State the preparation type.
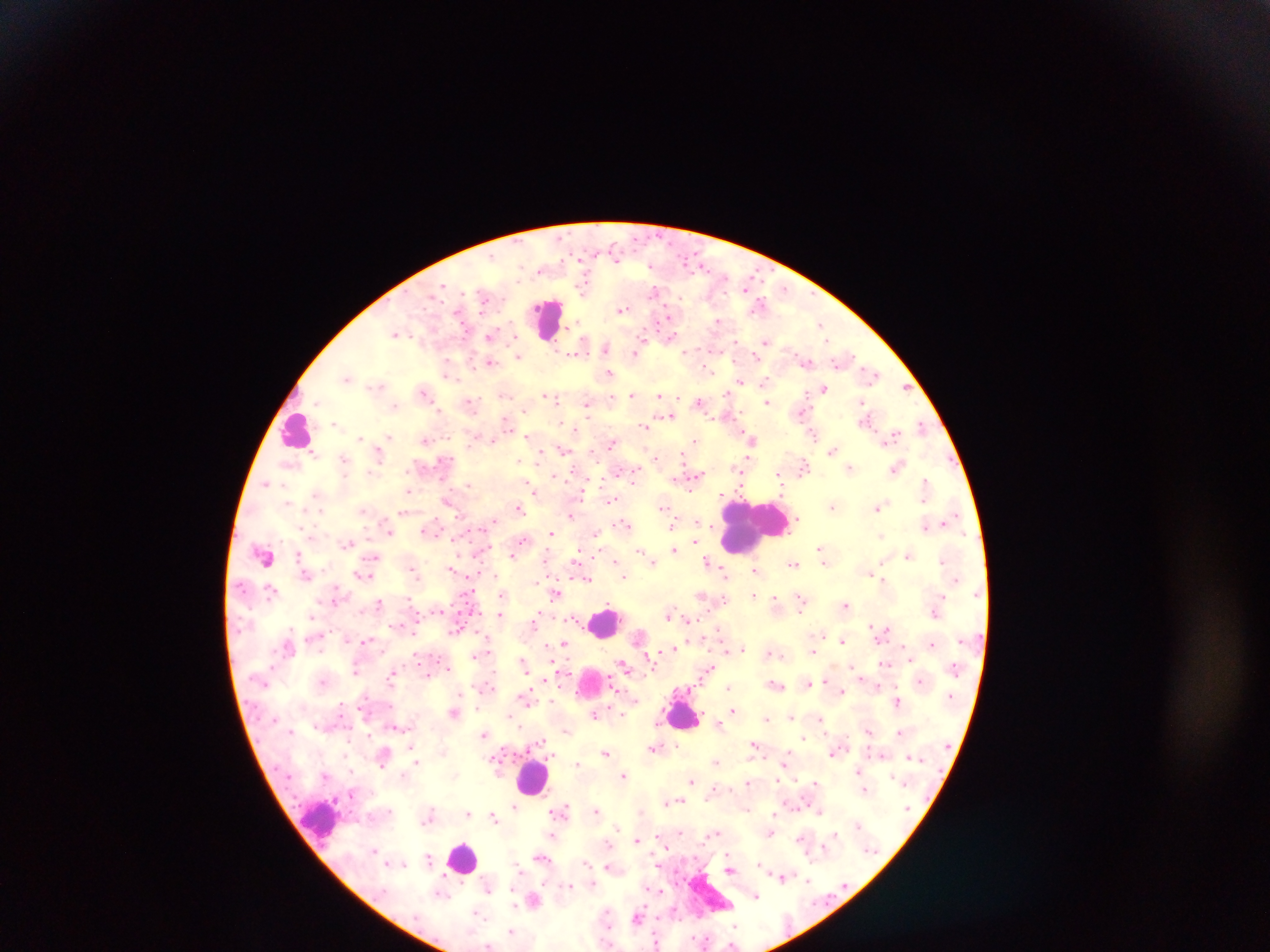
Thick blood film.

Approximate centers as (x, y) in pixels. Leukocyte locations: (548, 318), (296, 431), (753, 525), (605, 621), (591, 682), (684, 714), (533, 778), (320, 820), (463, 858), (713, 894). Plasmodium parasite locations: (584, 285), (655, 289), (759, 305), (622, 309), (670, 317), (718, 321), (821, 325), (396, 333), (491, 335), (670, 335), (766, 342), (579, 347), (606, 347), (639, 350), (518, 355), (491, 362), (805, 362), (448, 370), (609, 373), (871, 373), (347, 378), (741, 381), (764, 381), (379, 386), (905, 387), (824, 388), (424, 391), (632, 394), (727, 394), (660, 395), (551, 396), (612, 396), (556, 399), (699, 401), (768, 401), (862, 401), (471, 403), (588, 403), (394, 407), (668, 415), (867, 419), (507, 422), (337, 424), (644, 425), (921, 426), (575, 430), (813, 433), (528, 437), (891, 437), (389, 438), (361, 439), (695, 439), (751, 439), (425, 440), (492, 440), (613, 442), (563, 450), (832, 451), (314, 453), (379, 453), (656, 457), (344, 458), (521, 460), (804, 466), (897, 467), (850, 468), (741, 469), (371, 471), (634, 473), (779, 473), (554, 475), (695, 475), (266, 483), (468, 484), (926, 486), (408, 490), (534, 491), (317, 495), (611, 499), (448, 500), (832, 504), (663, 506), (519, 507), (879, 508), (363, 510), (404, 512), (571, 514), (698, 520), (944, 522), (625, 523), (708, 523), (672, 525), (925, 525), (430, 529), (389, 532), (551, 533), (597, 535), (881, 536), (456, 539), (523, 541), (347, 543), (675, 550), (821, 550), (641, 552), (299, 553), (264, 555), (513, 555), (909, 555), (580, 556), (615, 558), (651, 560), (707, 561), (794, 564), (452, 567), (413, 569), (755, 569), (725, 571), (870, 573), (306, 574), (623, 574), (364, 575), (586, 578), (884, 580), (270, 588), (470, 591), (557, 593), (502, 595), (754, 595), (703, 596), (801, 597), (409, 599), (775, 600), (378, 601), (845, 604), (439, 610), (935, 612), (670, 614), (500, 615), (313, 616), (539, 616), (536, 620), (687, 620), (399, 624), (458, 627), (882, 632), (640, 635), (346, 638), (366, 640), (841, 640), (932, 644), (564, 645), (673, 648), (741, 648), (726, 651), (669, 652), (771, 652), (813, 652), (477, 653), (909, 657), (651, 659), (523, 662), (885, 664), (624, 666), (448, 668), (355, 670), (707, 670), (393, 673), (826, 680), (322, 681), (807, 682), (776, 684), (876, 685), (729, 688), (842, 692), (365, 696), (526, 696), (553, 700), (898, 700), (732, 710), (455, 712), (622, 713), (595, 714), (791, 716), (767, 717), (820, 719), (718, 724), (520, 726), (567, 730), (868, 730), (899, 732), (485, 734), (803, 736), (539, 742), (678, 744), (755, 744), (654, 746), (411, 747), (605, 752), (835, 752), (345, 756), (383, 756), (910, 756), (498, 759), (417, 762), (716, 762), (784, 763), (576, 764), (859, 770), (623, 775), (693, 780), (815, 781), (749, 783), (865, 791), (679, 800), (669, 801), (514, 806), (560, 810), (597, 811), (820, 811), (468, 813), (775, 813), (494, 817), (679, 830), (716, 832), (770, 832), (835, 835), (552, 836), (659, 836), (802, 836), (637, 839), (608, 844), (728, 853), (542, 857), (429, 859), (585, 862), (402, 863), (760, 863), (609, 867), (730, 869), (782, 877), (808, 879), (591, 883), (650, 886), (489, 888), (660, 890), (440, 895), (755, 896), (534, 900), (476, 912), (638, 917), (512, 931), (657, 942), (488, 946). One field of view. Photographed through a microscope with a mobile-phone camera. Image is 1270×952 pixels. Sample from Ghana.